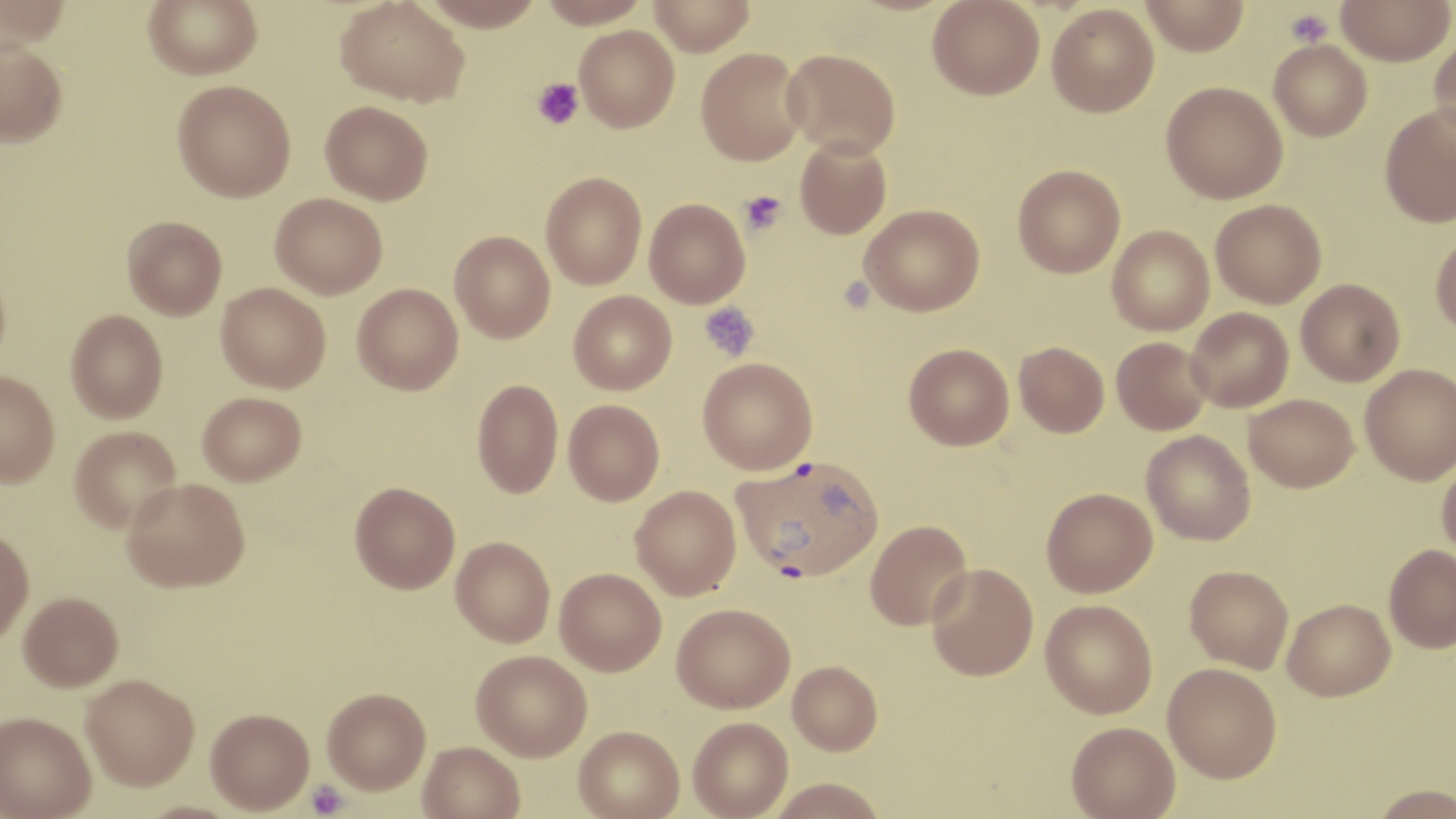

Approximate bounding boxes as named x1/y1/x2/y2 corners in pixels. Platelet locations: (x1=1286, y1=8, x2=1332, y2=47), (x1=532, y1=79, x2=583, y2=130), (x1=740, y1=190, x2=787, y2=236), (x1=699, y1=300, x2=759, y2=361), (x1=306, y1=780, x2=348, y2=818). Uninfected red blood cell locations: (x1=0, y1=0, x2=71, y2=50), (x1=143, y1=0, x2=262, y2=79), (x1=335, y1=0, x2=470, y2=107), (x1=537, y1=0, x2=652, y2=27), (x1=648, y1=0, x2=756, y2=56), (x1=928, y1=0, x2=1044, y2=100), (x1=1140, y1=0, x2=1250, y2=56), (x1=1336, y1=0, x2=1454, y2=66), (x1=419, y1=1, x2=545, y2=30), (x1=1047, y1=3, x2=1159, y2=117), (x1=574, y1=25, x2=680, y2=131), (x1=1428, y1=29, x2=1456, y2=143), (x1=0, y1=40, x2=68, y2=147), (x1=1268, y1=40, x2=1372, y2=141), (x1=696, y1=48, x2=807, y2=165), (x1=782, y1=49, x2=901, y2=158), (x1=172, y1=80, x2=296, y2=202), (x1=1161, y1=81, x2=1288, y2=203), (x1=320, y1=100, x2=433, y2=204), (x1=1379, y1=105, x2=1456, y2=227), (x1=795, y1=137, x2=891, y2=239), (x1=1012, y1=164, x2=1125, y2=278), (x1=541, y1=172, x2=646, y2=289), (x1=270, y1=193, x2=387, y2=298), (x1=644, y1=198, x2=750, y2=307), (x1=1210, y1=199, x2=1326, y2=308), (x1=859, y1=204, x2=985, y2=316), (x1=122, y1=216, x2=227, y2=320), (x1=1107, y1=225, x2=1214, y2=336), (x1=1430, y1=230, x2=1456, y2=336), (x1=450, y1=231, x2=556, y2=342), (x1=0, y1=258, x2=11, y2=375), (x1=1297, y1=279, x2=1405, y2=386), (x1=216, y1=282, x2=331, y2=393), (x1=352, y1=283, x2=463, y2=394), (x1=568, y1=291, x2=676, y2=395), (x1=1186, y1=307, x2=1294, y2=412), (x1=65, y1=310, x2=168, y2=423), (x1=1112, y1=337, x2=1212, y2=435), (x1=1014, y1=342, x2=1109, y2=437), (x1=904, y1=343, x2=1014, y2=450), (x1=698, y1=358, x2=817, y2=474), (x1=1360, y1=363, x2=1456, y2=485), (x1=0, y1=371, x2=60, y2=487), (x1=472, y1=379, x2=563, y2=498), (x1=198, y1=391, x2=306, y2=485), (x1=1244, y1=394, x2=1359, y2=492), (x1=563, y1=399, x2=665, y2=505), (x1=69, y1=425, x2=181, y2=532), (x1=1141, y1=430, x2=1255, y2=545), (x1=1437, y1=458, x2=1456, y2=561), (x1=122, y1=478, x2=250, y2=592), (x1=350, y1=481, x2=460, y2=593), (x1=630, y1=485, x2=741, y2=600), (x1=1041, y1=487, x2=1157, y2=597), (x1=864, y1=519, x2=972, y2=630), (x1=0, y1=527, x2=34, y2=645), (x1=451, y1=536, x2=555, y2=647), (x1=1384, y1=544, x2=1456, y2=652), (x1=926, y1=563, x2=1039, y2=680), (x1=1185, y1=565, x2=1293, y2=673), (x1=555, y1=568, x2=666, y2=676), (x1=18, y1=592, x2=124, y2=690), (x1=1283, y1=598, x2=1395, y2=700), (x1=1040, y1=600, x2=1157, y2=718), (x1=672, y1=603, x2=794, y2=712), (x1=471, y1=650, x2=592, y2=761), (x1=787, y1=661, x2=882, y2=755), (x1=1163, y1=662, x2=1282, y2=782), (x1=81, y1=674, x2=199, y2=790), (x1=322, y1=687, x2=431, y2=794), (x1=205, y1=708, x2=314, y2=814), (x1=0, y1=712, x2=97, y2=819), (x1=688, y1=717, x2=793, y2=819), (x1=1066, y1=721, x2=1180, y2=818), (x1=573, y1=725, x2=684, y2=819), (x1=418, y1=741, x2=525, y2=819), (x1=767, y1=778, x2=889, y2=819), (x1=1366, y1=784, x2=1456, y2=819). Plasmodium vivax-infected red blood cell locations: (x1=732, y1=455, x2=884, y2=582). Slide-level diagnosis: Plasmodium vivax. May-Grünwald-Giemsa-stained preparation. Thin blood film. Single field of view. 1000x magnification. Image is 1456×819 pixels. Light microscopy.